Assess the morphology of the erythrocytes.
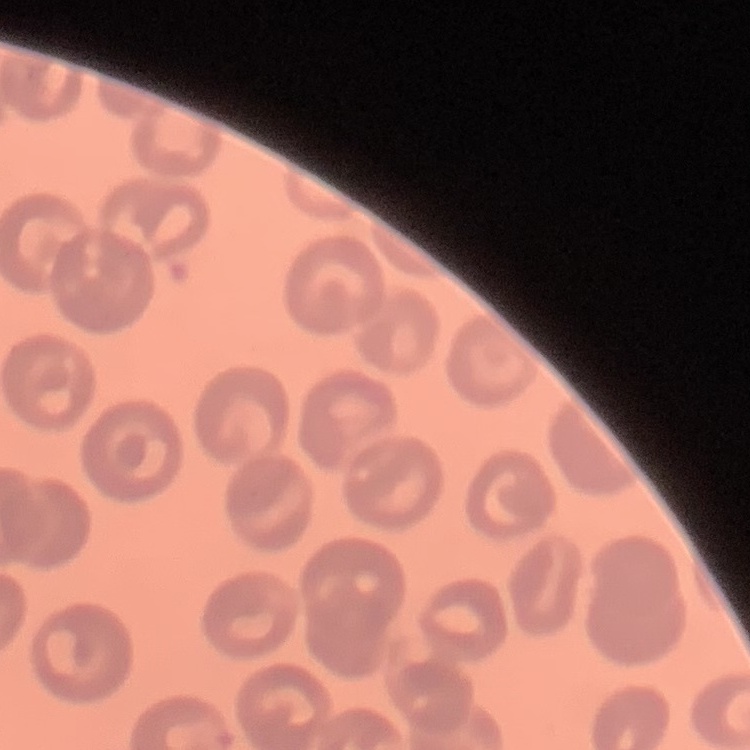

No rouleaux formation.

Field's or Giemsa stain. Thin peripheral smear. Square crop of a larger photomicrograph.